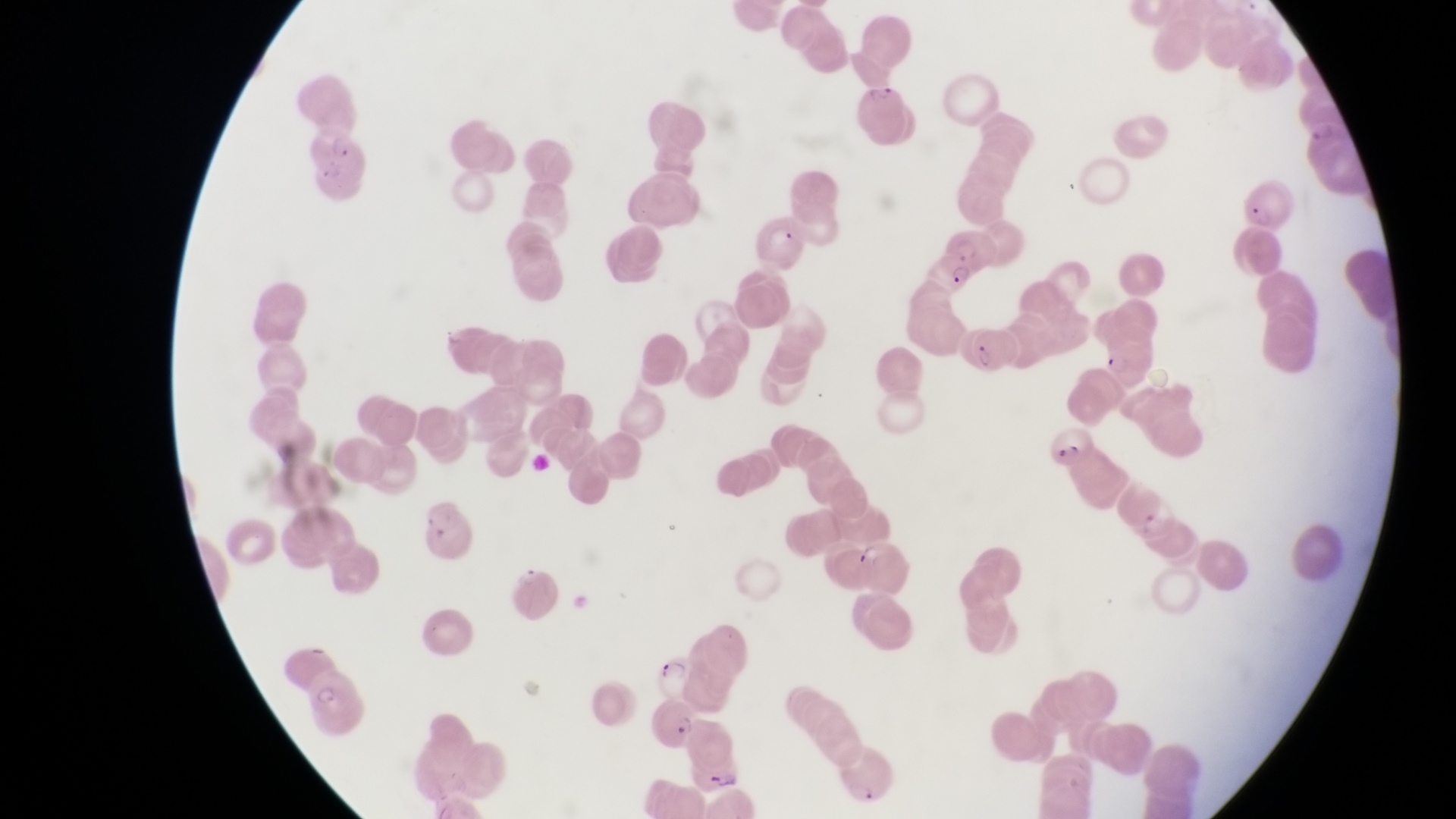
Approximate bounding boxes as [left, top, right, bottom] in pixels.
Summary:
  - Parasitised red blood cell locations: [310, 127, 374, 206], [1242, 178, 1289, 234], [756, 211, 806, 270], [933, 224, 997, 291], [962, 328, 1018, 365], [1046, 425, 1096, 472], [1118, 488, 1184, 547], [420, 495, 475, 566], [854, 538, 910, 596], [654, 654, 700, 699], [307, 667, 365, 730], [645, 698, 704, 748], [684, 748, 751, 800]
  - Magnification: 1000x
  - Country: Uganda
  - Capture: smartphone photograph through the eyepiece of an Olympus CX-23 microscope
  - Preparation: thin blood film
  - Field of view: single
  - Image size: 1456×819 pixels